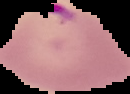
Summary:
  - Image type: cell region segmented out of the field of view; surrounding area masked to black
  - Malaria status: parasitized
  - Image size: 130×94 pixels
  - Preparation: thin blood smear